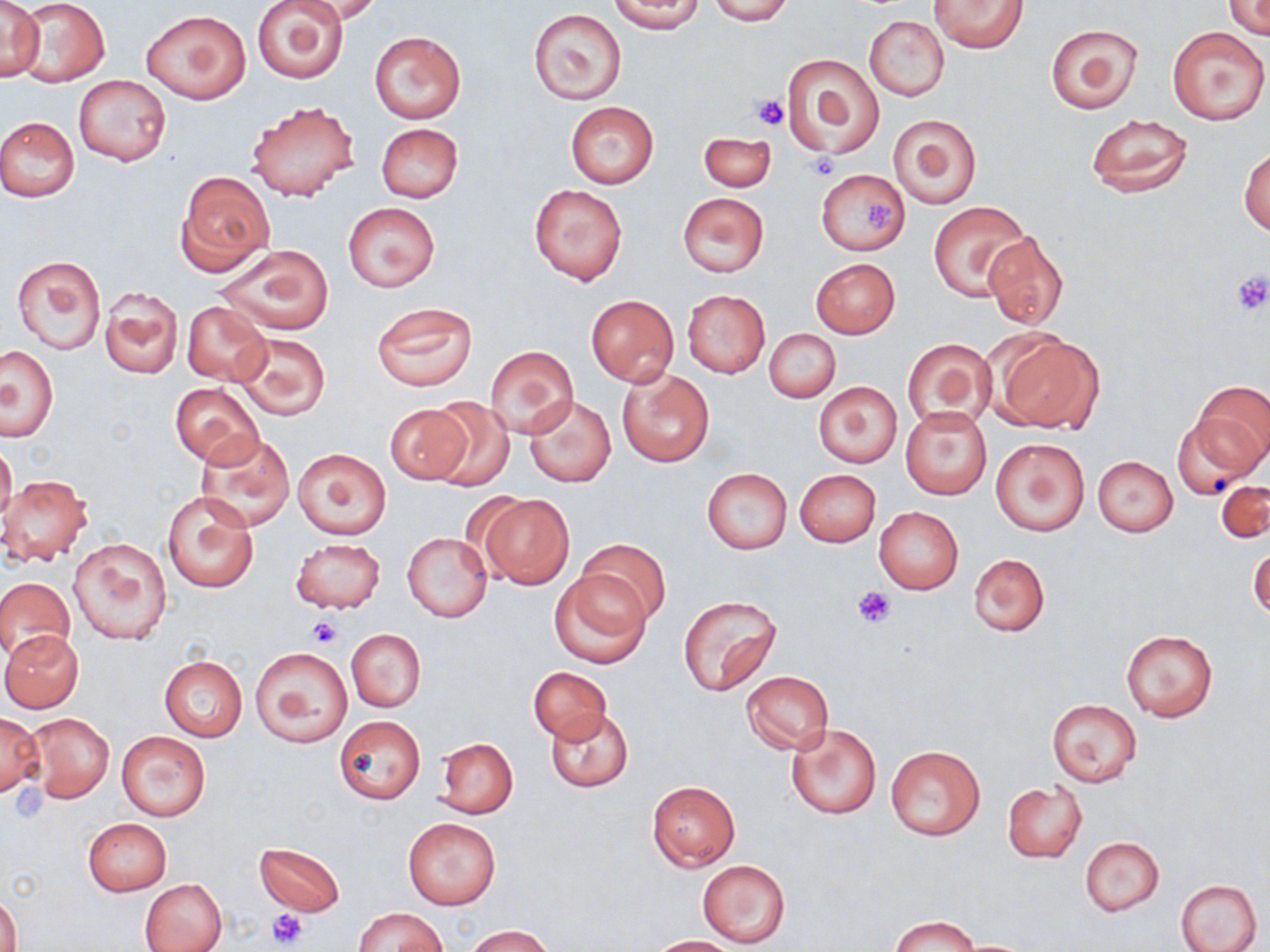
Approximate bounding boxes as (x1, y1, x2, y2) in pixels. Platelet locations: (754, 95, 789, 130), (806, 153, 839, 181), (864, 198, 898, 229), (1231, 270, 1270, 317), (853, 585, 896, 629), (309, 616, 339, 647), (8, 784, 51, 823), (266, 908, 309, 948). Uninfected red blood cell locations: (0, 0, 44, 80), (252, 0, 349, 84), (295, 0, 383, 23), (608, 0, 704, 33), (706, 0, 794, 24), (929, 1, 1027, 53), (1224, 1, 1270, 38), (13, 2, 111, 85), (528, 7, 626, 104), (142, 9, 250, 103), (865, 15, 950, 101), (1045, 22, 1143, 114), (1165, 25, 1268, 126), (369, 31, 465, 123), (779, 52, 884, 160), (73, 74, 172, 167), (247, 101, 359, 201), (565, 102, 659, 188), (887, 112, 982, 209), (1083, 112, 1194, 198), (0, 116, 80, 201), (376, 123, 463, 202), (697, 131, 775, 191), (1240, 144, 1269, 237), (816, 169, 909, 255), (175, 171, 274, 275), (528, 185, 628, 285), (678, 193, 769, 277), (343, 202, 439, 292), (928, 202, 1028, 301), (982, 232, 1069, 330), (214, 244, 335, 336), (11, 255, 106, 355), (811, 258, 900, 338), (99, 287, 184, 380), (684, 290, 770, 378), (586, 295, 678, 386), (182, 302, 271, 387), (370, 302, 477, 391), (764, 328, 840, 404), (232, 331, 331, 422), (990, 332, 1103, 433), (901, 339, 995, 431), (484, 344, 579, 438), (0, 345, 58, 440), (617, 368, 714, 467), (1192, 380, 1270, 474), (170, 382, 263, 467), (815, 382, 901, 467), (524, 395, 616, 488), (423, 400, 513, 489), (385, 403, 472, 483), (901, 407, 991, 500), (1171, 412, 1263, 500), (196, 433, 296, 531), (989, 437, 1090, 535), (0, 440, 18, 527), (291, 449, 390, 540), (1093, 455, 1177, 537), (702, 468, 792, 553), (795, 469, 881, 546), (1, 473, 94, 565), (1217, 478, 1269, 546), (161, 492, 259, 592), (477, 493, 574, 587), (874, 507, 963, 594), (403, 532, 491, 623), (291, 537, 386, 613), (576, 537, 670, 626), (67, 538, 171, 645), (1248, 542, 1269, 621), (970, 553, 1049, 637), (548, 572, 650, 669), (0, 577, 74, 660), (676, 593, 783, 696), (347, 629, 425, 712), (1120, 629, 1219, 722), (1, 631, 84, 712), (252, 647, 351, 746), (159, 656, 248, 740), (529, 667, 612, 742), (741, 671, 833, 754), (1047, 699, 1142, 786), (545, 709, 634, 792), (0, 711, 43, 798), (26, 714, 113, 802), (335, 716, 425, 803), (785, 721, 882, 819), (116, 730, 211, 821), (437, 738, 517, 818), (885, 745, 985, 839), (646, 781, 741, 871), (1002, 782, 1086, 864), (401, 815, 502, 910), (82, 816, 171, 895), (1080, 836, 1164, 916), (254, 842, 346, 916), (698, 860, 790, 947), (139, 878, 227, 952), (1175, 878, 1261, 952), (1, 894, 22, 952), (354, 907, 448, 952), (891, 915, 978, 952), (465, 925, 553, 951), (646, 935, 739, 951). Slide-level diagnosis: negative for blood parasites. Thin blood film. Optical microscopy. One field of a larger specimen. Captured at 1000x magnification. May-Grünwald-Giemsa stain. Image is 1270×952 pixels.